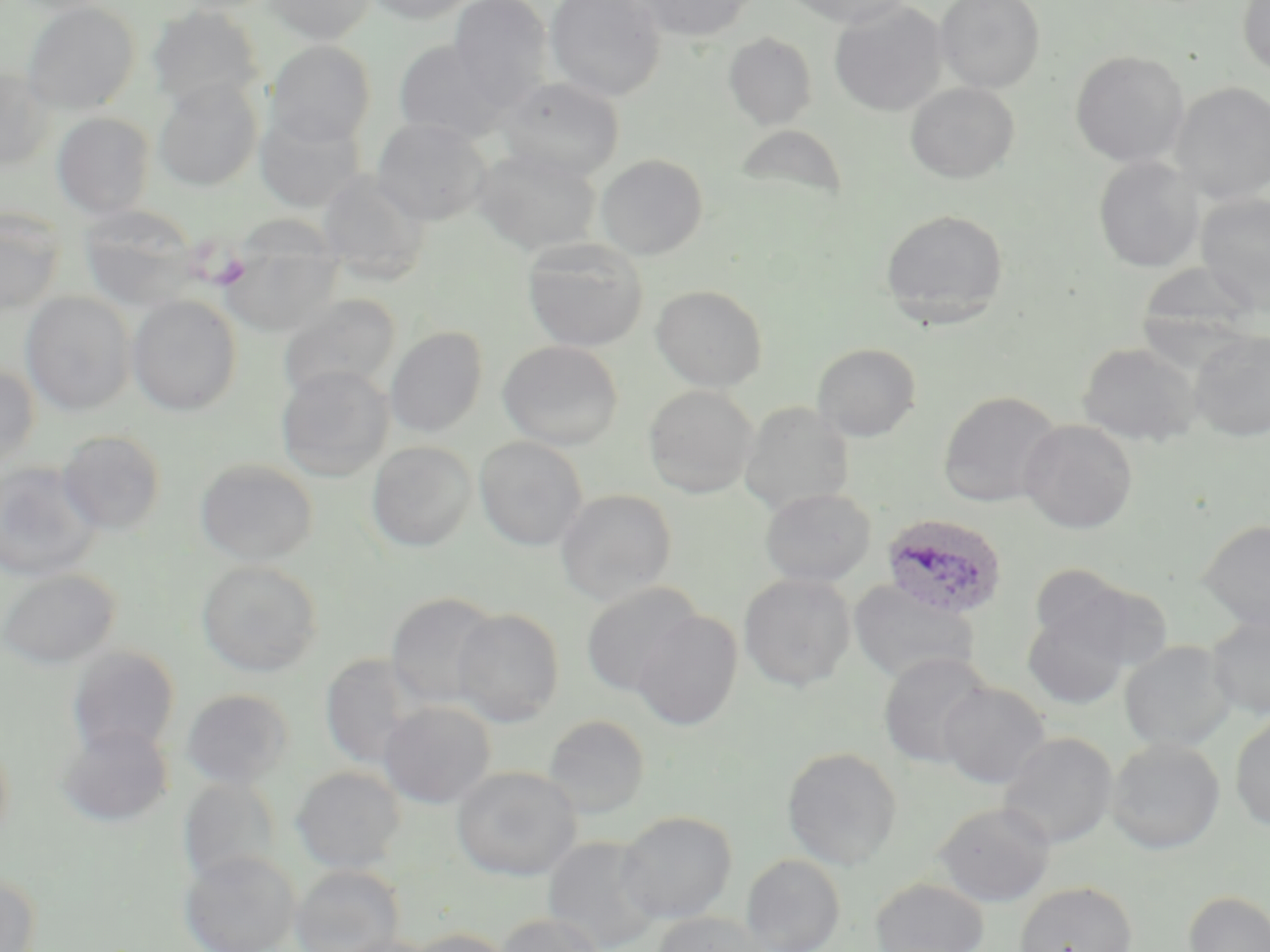

Summary:
  - Coordinate format: approximate bounding boxes as named x1/y1/x2/y2 corners in pixels
  - Platelet locations: (x1=211, y1=251, x2=251, y2=289)
  - Plasmodium ovale-infected red blood cell locations: (x1=881, y1=513, x2=1008, y2=620)
  - Uninfected red blood cell locations: (x1=263, y1=0, x2=378, y2=44), (x1=365, y1=0, x2=477, y2=24), (x1=448, y1=0, x2=553, y2=109), (x1=544, y1=0, x2=667, y2=101), (x1=783, y1=0, x2=914, y2=28), (x1=935, y1=0, x2=1046, y2=93), (x1=1237, y1=0, x2=1270, y2=77), (x1=21, y1=1, x2=141, y2=114), (x1=634, y1=1, x2=757, y2=41), (x1=829, y1=1, x2=947, y2=117), (x1=147, y1=5, x2=265, y2=111), (x1=723, y1=33, x2=818, y2=131), (x1=265, y1=39, x2=376, y2=147), (x1=392, y1=39, x2=512, y2=142), (x1=1070, y1=50, x2=1189, y2=167), (x1=0, y1=68, x2=53, y2=171), (x1=152, y1=76, x2=263, y2=192), (x1=495, y1=76, x2=624, y2=180), (x1=905, y1=82, x2=1020, y2=184), (x1=1171, y1=82, x2=1270, y2=203), (x1=253, y1=108, x2=366, y2=213), (x1=52, y1=112, x2=156, y2=219), (x1=371, y1=118, x2=492, y2=225), (x1=733, y1=123, x2=849, y2=212), (x1=473, y1=147, x2=602, y2=254), (x1=596, y1=154, x2=708, y2=260), (x1=1093, y1=156, x2=1204, y2=273), (x1=316, y1=168, x2=430, y2=283), (x1=1196, y1=193, x2=1270, y2=314), (x1=78, y1=204, x2=201, y2=311), (x1=880, y1=208, x2=1009, y2=325), (x1=0, y1=209, x2=65, y2=314), (x1=220, y1=224, x2=346, y2=336), (x1=522, y1=239, x2=649, y2=352), (x1=1135, y1=263, x2=1262, y2=356), (x1=651, y1=285, x2=768, y2=391), (x1=20, y1=291, x2=136, y2=416), (x1=127, y1=294, x2=243, y2=416), (x1=278, y1=294, x2=401, y2=400), (x1=385, y1=326, x2=488, y2=437), (x1=1189, y1=329, x2=1270, y2=441), (x1=498, y1=340, x2=623, y2=450), (x1=1078, y1=342, x2=1201, y2=446), (x1=812, y1=343, x2=921, y2=442), (x1=0, y1=364, x2=40, y2=475), (x1=276, y1=365, x2=394, y2=482), (x1=643, y1=385, x2=758, y2=498), (x1=937, y1=390, x2=1062, y2=508), (x1=739, y1=403, x2=855, y2=516), (x1=1019, y1=419, x2=1138, y2=534), (x1=56, y1=430, x2=168, y2=535), (x1=475, y1=436, x2=588, y2=551), (x1=367, y1=441, x2=478, y2=552), (x1=195, y1=458, x2=319, y2=565), (x1=0, y1=460, x2=103, y2=582), (x1=759, y1=487, x2=876, y2=587), (x1=556, y1=488, x2=677, y2=605), (x1=1198, y1=519, x2=1270, y2=632), (x1=196, y1=559, x2=323, y2=677), (x1=1027, y1=563, x2=1136, y2=655), (x1=0, y1=569, x2=120, y2=670), (x1=738, y1=573, x2=856, y2=691), (x1=1057, y1=577, x2=1172, y2=674), (x1=849, y1=580, x2=980, y2=686), (x1=581, y1=582, x2=703, y2=697), (x1=385, y1=592, x2=502, y2=709), (x1=1022, y1=604, x2=1132, y2=710), (x1=451, y1=607, x2=564, y2=727), (x1=631, y1=611, x2=742, y2=731), (x1=1206, y1=613, x2=1270, y2=719), (x1=1119, y1=640, x2=1236, y2=752), (x1=66, y1=645, x2=181, y2=758), (x1=878, y1=652, x2=993, y2=768), (x1=320, y1=654, x2=421, y2=768), (x1=938, y1=681, x2=1051, y2=788), (x1=180, y1=688, x2=294, y2=789), (x1=378, y1=701, x2=496, y2=808), (x1=1230, y1=713, x2=1270, y2=832), (x1=543, y1=714, x2=650, y2=818), (x1=56, y1=723, x2=173, y2=828), (x1=0, y1=726, x2=14, y2=851), (x1=998, y1=732, x2=1118, y2=848), (x1=1106, y1=737, x2=1225, y2=854), (x1=782, y1=747, x2=902, y2=870), (x1=291, y1=766, x2=407, y2=873), (x1=451, y1=766, x2=583, y2=881), (x1=178, y1=777, x2=282, y2=888), (x1=934, y1=801, x2=1055, y2=907), (x1=616, y1=810, x2=737, y2=924), (x1=542, y1=835, x2=664, y2=952), (x1=179, y1=850, x2=300, y2=952), (x1=741, y1=854, x2=846, y2=952), (x1=291, y1=864, x2=404, y2=952), (x1=0, y1=871, x2=42, y2=952), (x1=871, y1=877, x2=989, y2=952), (x1=1014, y1=881, x2=1137, y2=952), (x1=1183, y1=890, x2=1270, y2=952), (x1=654, y1=912, x2=770, y2=952), (x1=494, y1=913, x2=607, y2=952), (x1=404, y1=928, x2=516, y2=952), (x1=332, y1=935, x2=438, y2=952)
  - Slide-level diagnosis: Plasmodium ovale
  - Magnification: 1000x
  - Modality: light microscopy
  - Preparation: thin blood smear
  - Image size: 1270×952 pixels
  - Field of view: single
  - Stain: May-Grünwald-Giemsa